Outline each Plasmodium falciparum-infected red blood cell.
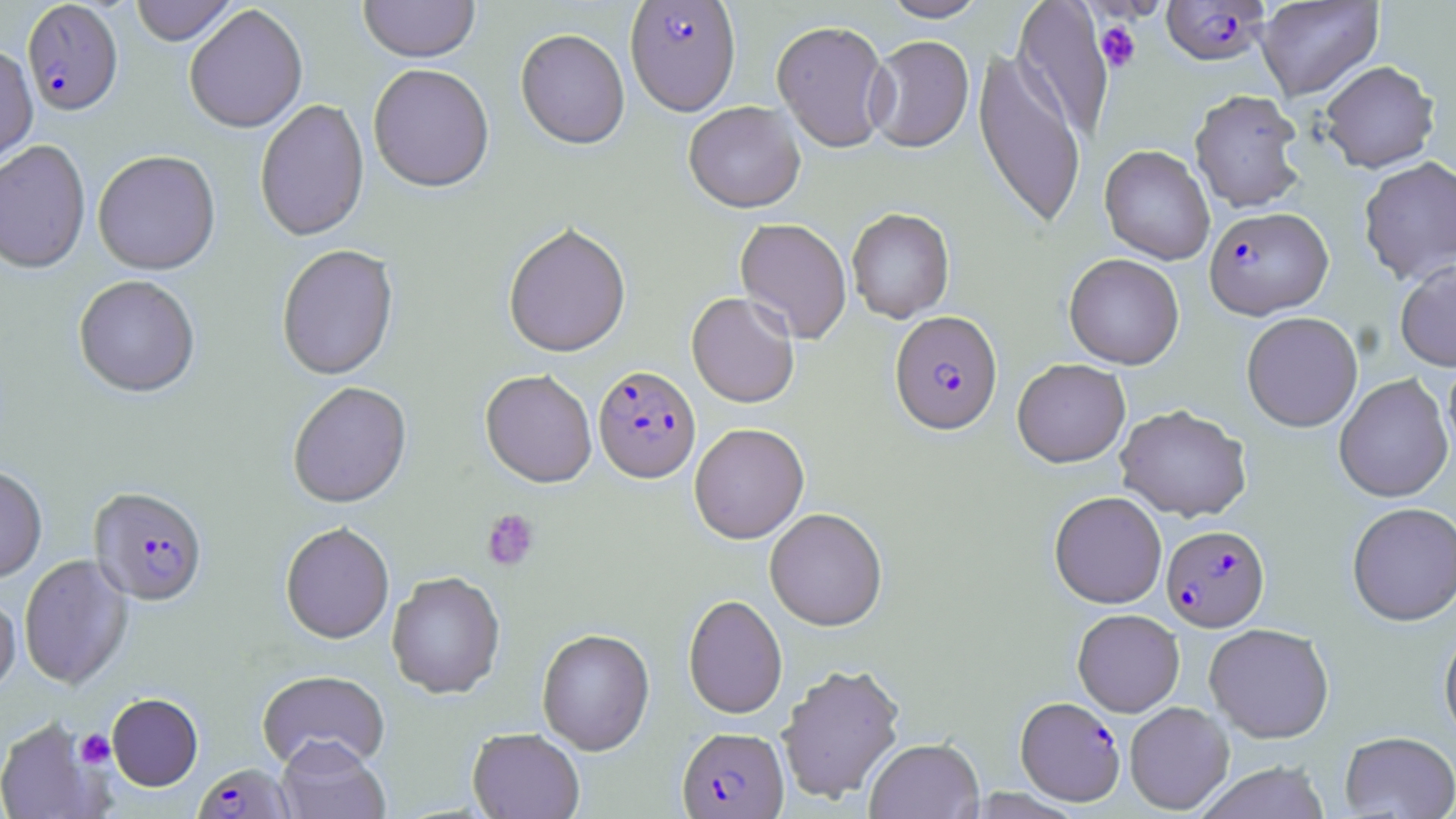
Approximate bounding boxes as named x1/y1/x2/y2 corners in pixels.
Plasmodium falciparum-infected red blood cells: (x1=625, y1=1, x2=741, y2=120), (x1=1161, y1=1, x2=1270, y2=66), (x1=22, y1=2, x2=124, y2=118), (x1=1204, y1=206, x2=1333, y2=319), (x1=889, y1=312, x2=1003, y2=436), (x1=593, y1=367, x2=701, y2=485), (x1=88, y1=488, x2=209, y2=608), (x1=1161, y1=524, x2=1271, y2=632), (x1=1015, y1=697, x2=1125, y2=805), (x1=677, y1=728, x2=788, y2=818), (x1=192, y1=763, x2=295, y2=819).

slide-level diagnosis = Plasmodium falciparum
modality = light microscopy
preparation = thin blood smear
stain = May-Grünwald-Giemsa
platelet locations = approximate bounding boxes as named x1/y1/x2/y2 corners in pixels: (x1=1095, y1=21, x2=1142, y2=72), (x1=482, y1=509, x2=540, y2=571), (x1=75, y1=729, x2=115, y2=768)
field of view = single
uninfected red blood cell locations = approximate bounding boxes as named x1/y1/x2/y2 corners in pixels: (x1=130, y1=0, x2=238, y2=47), (x1=358, y1=0, x2=480, y2=66), (x1=880, y1=0, x2=989, y2=23), (x1=1012, y1=0, x2=1115, y2=140), (x1=1255, y1=0, x2=1384, y2=100), (x1=184, y1=6, x2=308, y2=135), (x1=771, y1=22, x2=892, y2=154), (x1=515, y1=31, x2=629, y2=153), (x1=865, y1=37, x2=974, y2=155), (x1=0, y1=47, x2=38, y2=171), (x1=973, y1=49, x2=1086, y2=232), (x1=1319, y1=60, x2=1439, y2=172), (x1=368, y1=66, x2=495, y2=197), (x1=1189, y1=89, x2=1307, y2=213), (x1=255, y1=100, x2=370, y2=244), (x1=683, y1=103, x2=806, y2=216), (x1=0, y1=143, x2=91, y2=276), (x1=1099, y1=145, x2=1215, y2=265), (x1=93, y1=152, x2=221, y2=277), (x1=1358, y1=156, x2=1456, y2=284), (x1=846, y1=209, x2=955, y2=324), (x1=735, y1=219, x2=852, y2=344), (x1=503, y1=225, x2=632, y2=361), (x1=276, y1=246, x2=399, y2=382), (x1=1064, y1=253, x2=1184, y2=369), (x1=1395, y1=260, x2=1456, y2=371), (x1=73, y1=277, x2=200, y2=400), (x1=686, y1=293, x2=799, y2=409), (x1=1241, y1=312, x2=1363, y2=432), (x1=1443, y1=351, x2=1456, y2=466), (x1=1012, y1=359, x2=1130, y2=468), (x1=480, y1=372, x2=597, y2=490), (x1=1334, y1=374, x2=1453, y2=503), (x1=288, y1=383, x2=412, y2=510), (x1=1115, y1=404, x2=1252, y2=522), (x1=689, y1=424, x2=810, y2=546), (x1=0, y1=467, x2=47, y2=584), (x1=1049, y1=491, x2=1167, y2=609), (x1=1346, y1=502, x2=1456, y2=626), (x1=765, y1=508, x2=888, y2=632), (x1=280, y1=524, x2=395, y2=646), (x1=19, y1=555, x2=134, y2=691), (x1=387, y1=573, x2=506, y2=701), (x1=0, y1=595, x2=21, y2=700), (x1=683, y1=595, x2=787, y2=720), (x1=1072, y1=608, x2=1185, y2=716), (x1=1204, y1=623, x2=1334, y2=743), (x1=1439, y1=625, x2=1456, y2=746), (x1=536, y1=630, x2=655, y2=756), (x1=776, y1=662, x2=906, y2=805), (x1=257, y1=671, x2=390, y2=774), (x1=107, y1=694, x2=203, y2=792), (x1=1124, y1=701, x2=1234, y2=814), (x1=0, y1=717, x2=106, y2=819), (x1=468, y1=729, x2=584, y2=819), (x1=1339, y1=731, x2=1456, y2=818), (x1=865, y1=738, x2=984, y2=819), (x1=277, y1=740, x2=390, y2=819), (x1=1194, y1=761, x2=1331, y2=819)
image size = 1456×819 pixels
magnification = 1000x